Give the extent of all Plasmodium falciparum-infected red blood cells.
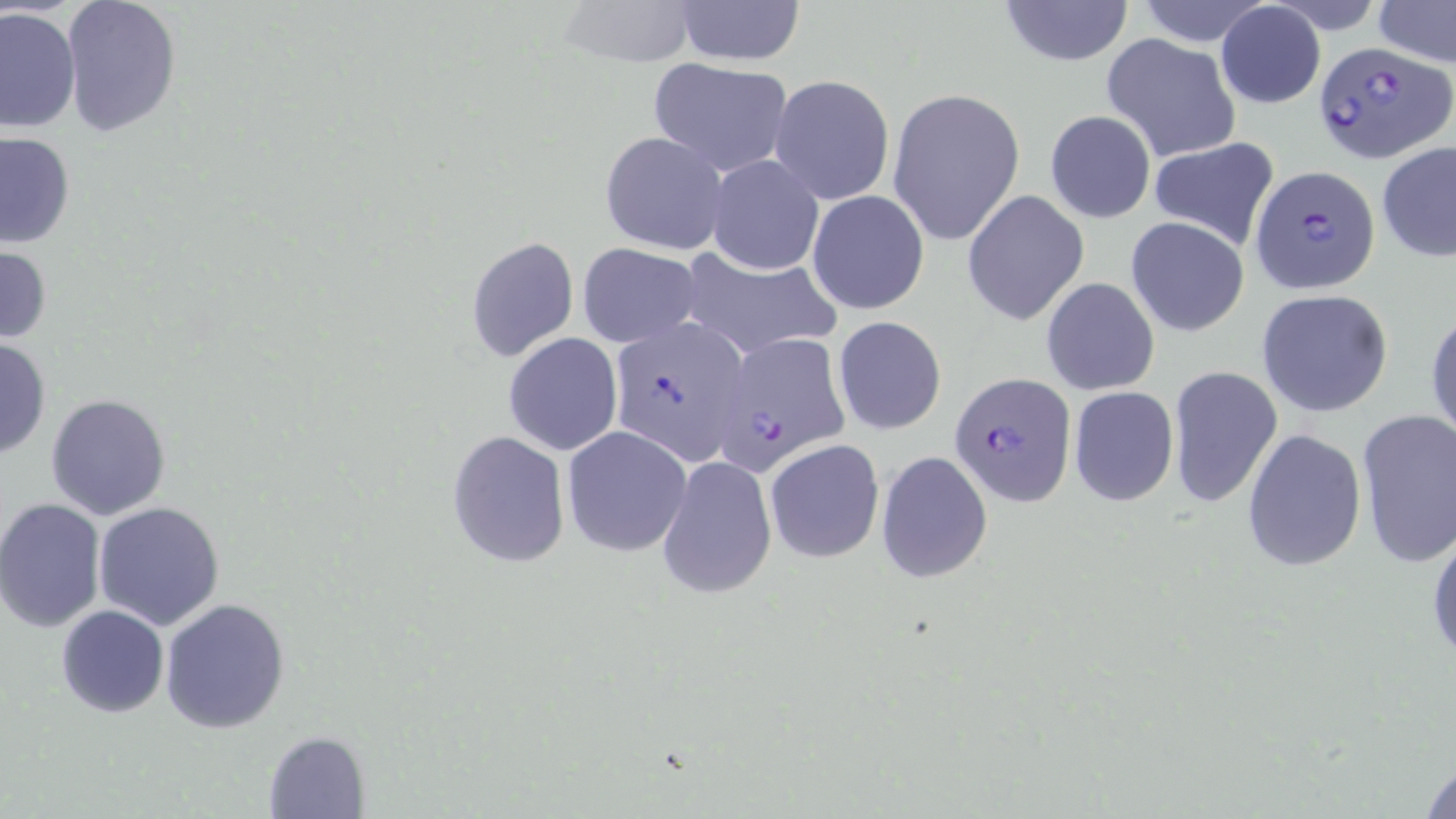

Approximate bounding boxes as (x1, y1, x2, y2) in pixels.
Plasmodium falciparum-infected red blood cells: (1314, 38, 1452, 166), (1250, 166, 1380, 294), (608, 316, 751, 464), (711, 333, 852, 475), (949, 371, 1075, 503).

Uninfected red blood cell locations: (60, 0, 182, 137), (555, 0, 700, 69), (672, 0, 806, 66), (996, 0, 1135, 68), (1134, 0, 1273, 46), (1373, 0, 1455, 68), (1214, 3, 1326, 108), (1, 6, 81, 134), (1101, 33, 1241, 163), (647, 57, 794, 177), (768, 75, 895, 206), (886, 87, 1026, 247), (1044, 109, 1156, 224), (0, 130, 76, 249), (599, 130, 729, 256), (1146, 136, 1281, 251), (1377, 141, 1456, 263), (708, 155, 823, 275), (807, 189, 931, 315), (962, 189, 1089, 325), (1125, 216, 1250, 337), (466, 236, 579, 362), (576, 243, 703, 348), (0, 244, 52, 344), (673, 248, 838, 360), (1041, 277, 1159, 395), (1256, 290, 1394, 417), (1426, 301, 1456, 448), (831, 315, 946, 434), (503, 332, 623, 456), (0, 337, 51, 460), (1168, 366, 1283, 508), (1068, 385, 1179, 507), (44, 393, 171, 521), (1355, 407, 1456, 567), (561, 425, 692, 557), (1241, 428, 1367, 572), (446, 431, 570, 568), (766, 440, 885, 562), (876, 451, 994, 583), (655, 455, 777, 600), (0, 497, 106, 633), (93, 500, 225, 631), (1427, 519, 1456, 668), (159, 599, 291, 735), (56, 605, 169, 717), (262, 731, 368, 819), (1418, 752, 1456, 818). Slide-level diagnosis: Plasmodium falciparum. Single field of view. 1000x magnification. Image is 1456×819 pixels. Thin blood film. Optical microscopy. May-Grünwald-Giemsa stain.